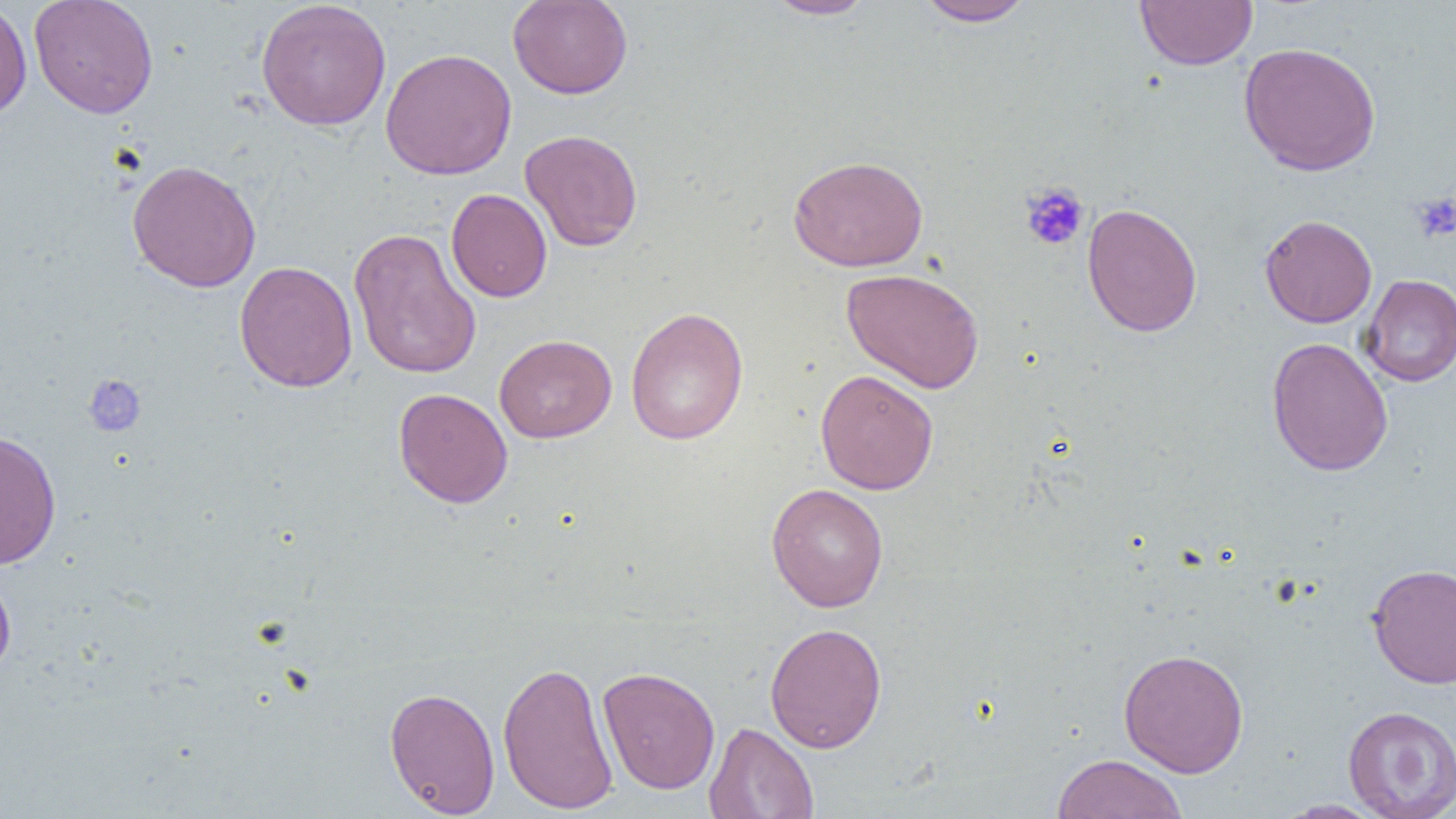

Summary:
  - Coordinate format: approximate bounding boxes as (x1,y1)-(x2,y2) corner pairs in pixels
  - Platelet locations: (1020,182)-(1089,252), (1411,192)-(1456,243), (83,374)-(147,437)
  - Uninfected red blood cell locations: (0,0)-(32,123), (29,0)-(158,118), (507,0)-(633,99), (763,0)-(879,20), (914,0)-(1037,27), (1134,0)-(1257,71), (256,1)-(392,131), (1238,42)-(1381,177), (380,48)-(517,180), (520,130)-(643,252), (788,154)-(929,272), (126,159)-(261,292), (446,189)-(552,302), (1082,203)-(1202,337), (1260,214)-(1377,328), (348,227)-(482,380), (234,260)-(358,393), (841,268)-(985,394), (1359,274)-(1456,387), (625,307)-(749,445), (494,334)-(617,443), (1266,337)-(1394,477), (815,369)-(939,495), (393,387)-(513,508), (0,430)-(62,569), (766,483)-(889,612), (1366,562)-(1456,688), (0,566)-(16,678), (765,622)-(887,752), (1118,648)-(1249,778), (497,659)-(618,814), (598,666)-(720,794), (384,686)-(500,817), (1342,705)-(1456,818), (703,722)-(819,818), (1052,753)-(1188,819), (1276,799)-(1388,818)
  - Slide-level diagnosis: negative for blood parasites
  - Preparation: thin blood smear
  - Modality: light microscopy
  - Magnification: 1000x
  - Field of view: single
  - Image size: 1456×819 pixels